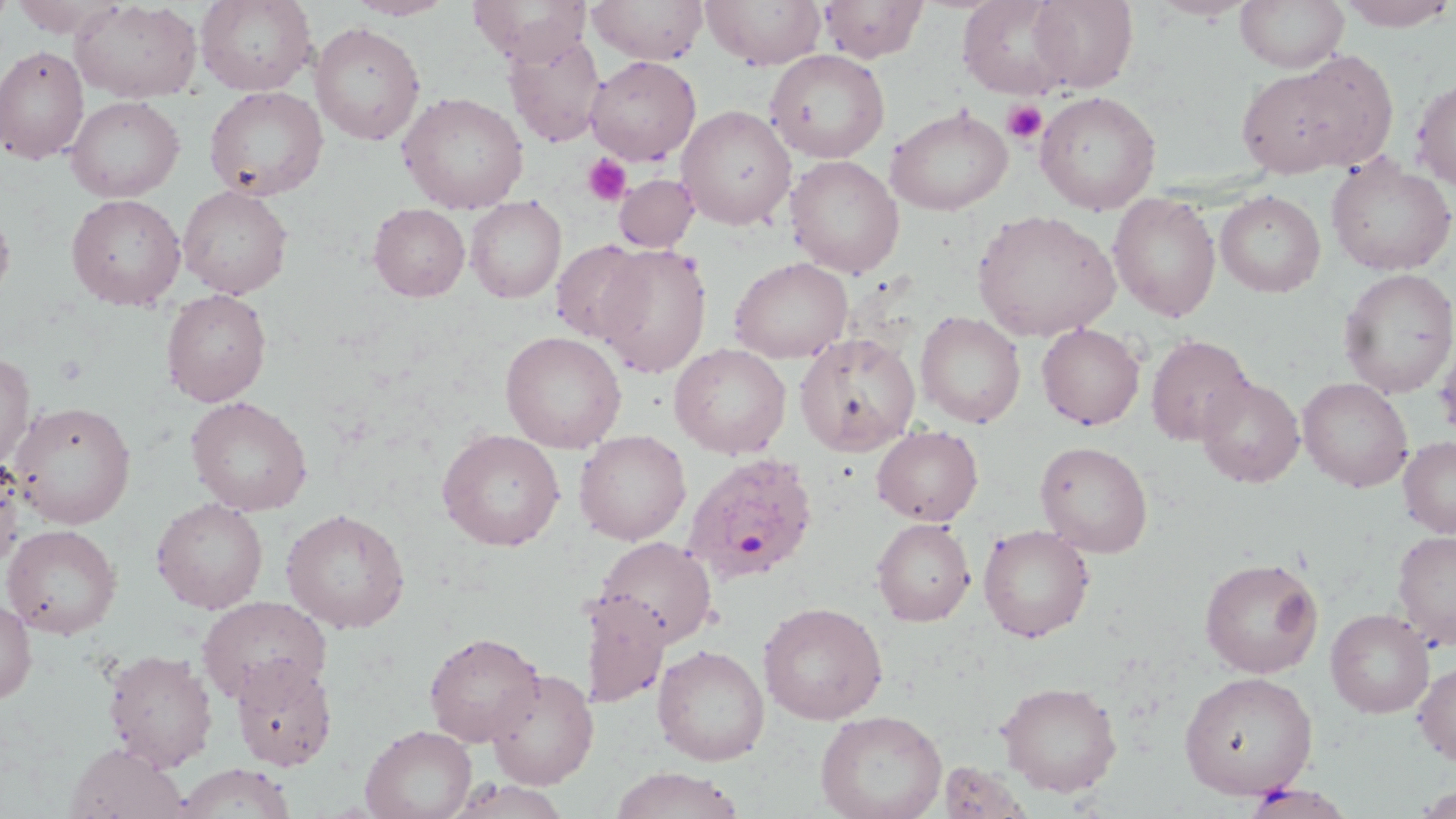

Approximate bounding boxes as named x1/y1/x2/y2 corners in pixels. Uninfected red blood cell locations: (x1=70, y1=0, x2=202, y2=103), (x1=195, y1=0, x2=317, y2=95), (x1=346, y1=0, x2=458, y2=20), (x1=468, y1=0, x2=590, y2=65), (x1=588, y1=0, x2=708, y2=64), (x1=701, y1=0, x2=828, y2=69), (x1=818, y1=0, x2=930, y2=62), (x1=958, y1=0, x2=1074, y2=99), (x1=1151, y1=0, x2=1255, y2=21), (x1=1236, y1=0, x2=1349, y2=73), (x1=1336, y1=0, x2=1456, y2=31), (x1=10, y1=1, x2=122, y2=37), (x1=1027, y1=1, x2=1139, y2=92), (x1=310, y1=22, x2=425, y2=146), (x1=503, y1=32, x2=605, y2=147), (x1=0, y1=45, x2=89, y2=164), (x1=765, y1=49, x2=890, y2=163), (x1=1237, y1=54, x2=1398, y2=179), (x1=585, y1=56, x2=701, y2=165), (x1=1412, y1=76, x2=1456, y2=190), (x1=204, y1=86, x2=328, y2=200), (x1=1035, y1=90, x2=1161, y2=215), (x1=398, y1=91, x2=529, y2=214), (x1=65, y1=96, x2=184, y2=202), (x1=677, y1=105, x2=796, y2=230), (x1=886, y1=105, x2=1013, y2=215), (x1=786, y1=155, x2=904, y2=278), (x1=1326, y1=156, x2=1456, y2=275), (x1=614, y1=173, x2=699, y2=253), (x1=178, y1=185, x2=293, y2=298), (x1=1215, y1=190, x2=1326, y2=297), (x1=66, y1=193, x2=185, y2=310), (x1=1108, y1=193, x2=1221, y2=322), (x1=466, y1=196, x2=566, y2=303), (x1=0, y1=202, x2=16, y2=307), (x1=368, y1=203, x2=470, y2=301), (x1=973, y1=210, x2=1121, y2=341), (x1=550, y1=239, x2=653, y2=345), (x1=594, y1=243, x2=712, y2=378), (x1=729, y1=257, x2=853, y2=363), (x1=1338, y1=268, x2=1456, y2=398), (x1=161, y1=289, x2=271, y2=406), (x1=916, y1=311, x2=1025, y2=428), (x1=1036, y1=323, x2=1145, y2=430), (x1=500, y1=331, x2=627, y2=453), (x1=795, y1=332, x2=920, y2=456), (x1=1146, y1=335, x2=1254, y2=446), (x1=669, y1=343, x2=792, y2=459), (x1=0, y1=351, x2=36, y2=470), (x1=1196, y1=376, x2=1304, y2=488), (x1=1298, y1=377, x2=1413, y2=491), (x1=186, y1=396, x2=313, y2=515), (x1=10, y1=401, x2=136, y2=528), (x1=872, y1=425, x2=983, y2=526), (x1=437, y1=429, x2=565, y2=551), (x1=574, y1=430, x2=691, y2=545), (x1=1398, y1=436, x2=1456, y2=538), (x1=1035, y1=441, x2=1153, y2=557), (x1=0, y1=453, x2=26, y2=572), (x1=151, y1=497, x2=268, y2=614), (x1=280, y1=508, x2=410, y2=633), (x1=872, y1=518, x2=975, y2=626), (x1=2, y1=524, x2=122, y2=639), (x1=978, y1=524, x2=1094, y2=642), (x1=1392, y1=528, x2=1456, y2=650), (x1=594, y1=536, x2=716, y2=647), (x1=1199, y1=556, x2=1323, y2=677), (x1=580, y1=590, x2=671, y2=711), (x1=197, y1=595, x2=331, y2=705), (x1=0, y1=598, x2=36, y2=704), (x1=758, y1=601, x2=887, y2=724), (x1=1326, y1=608, x2=1435, y2=717), (x1=424, y1=631, x2=545, y2=747), (x1=652, y1=644, x2=770, y2=765), (x1=103, y1=649, x2=218, y2=771), (x1=231, y1=657, x2=338, y2=770), (x1=1413, y1=659, x2=1456, y2=765), (x1=486, y1=667, x2=599, y2=788), (x1=1179, y1=671, x2=1318, y2=799), (x1=997, y1=680, x2=1122, y2=797), (x1=815, y1=709, x2=947, y2=819), (x1=360, y1=724, x2=477, y2=819), (x1=64, y1=742, x2=188, y2=819), (x1=938, y1=761, x2=1031, y2=818), (x1=175, y1=763, x2=296, y2=819), (x1=608, y1=767, x2=747, y2=819), (x1=446, y1=778, x2=573, y2=819), (x1=1242, y1=782, x2=1355, y2=819), (x1=1414, y1=786, x2=1455, y2=818). Platelet locations: (x1=1002, y1=100, x2=1047, y2=145), (x1=583, y1=155, x2=630, y2=206). Plasmodium ovale-infected red blood cell locations: (x1=682, y1=452, x2=819, y2=586). Slide-level diagnosis: Plasmodium ovale. Image is 1456×819 pixels. Light microscopy. Thin blood smear. One field of a larger specimen. Captured at 1000x magnification. May-Grünwald-Giemsa-stained preparation.